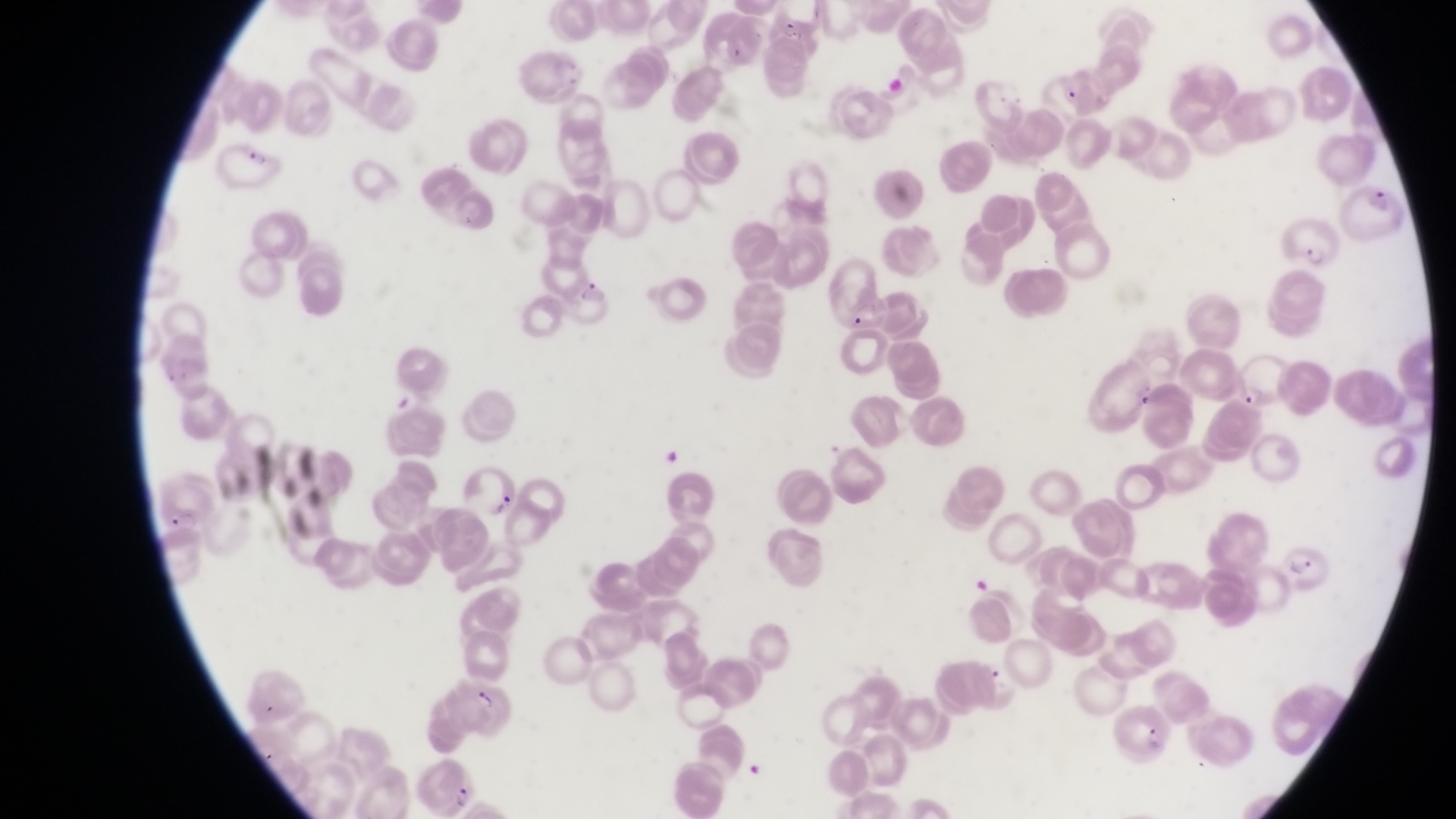

{
  "preparation": "thin blood film",
  "magnification": "1000x",
  "field_of_view": "single",
  "capture": "smartphone photograph through the eyepiece of an Olympus CX-23 microscope",
  "image_size": "1456×819 pixels",
  "parasitised_red_blood_cell_locations": "approximate bounding boxes as left top right bottom in pixels: 215 138 284 193; 1348 175 1407 247; 1281 212 1344 268; 555 270 611 329; 1232 344 1292 411; 462 462 525 522; 1276 538 1332 594; 446 670 515 737; 1109 698 1170 762; 416 759 477 815",
  "artifact_platelet_like_body_stain_precipitate_or_debris_locations": "approximate bounding boxes as left top right bottom in pixels: 661 444 680 465",
  "country": "Uganda"
}